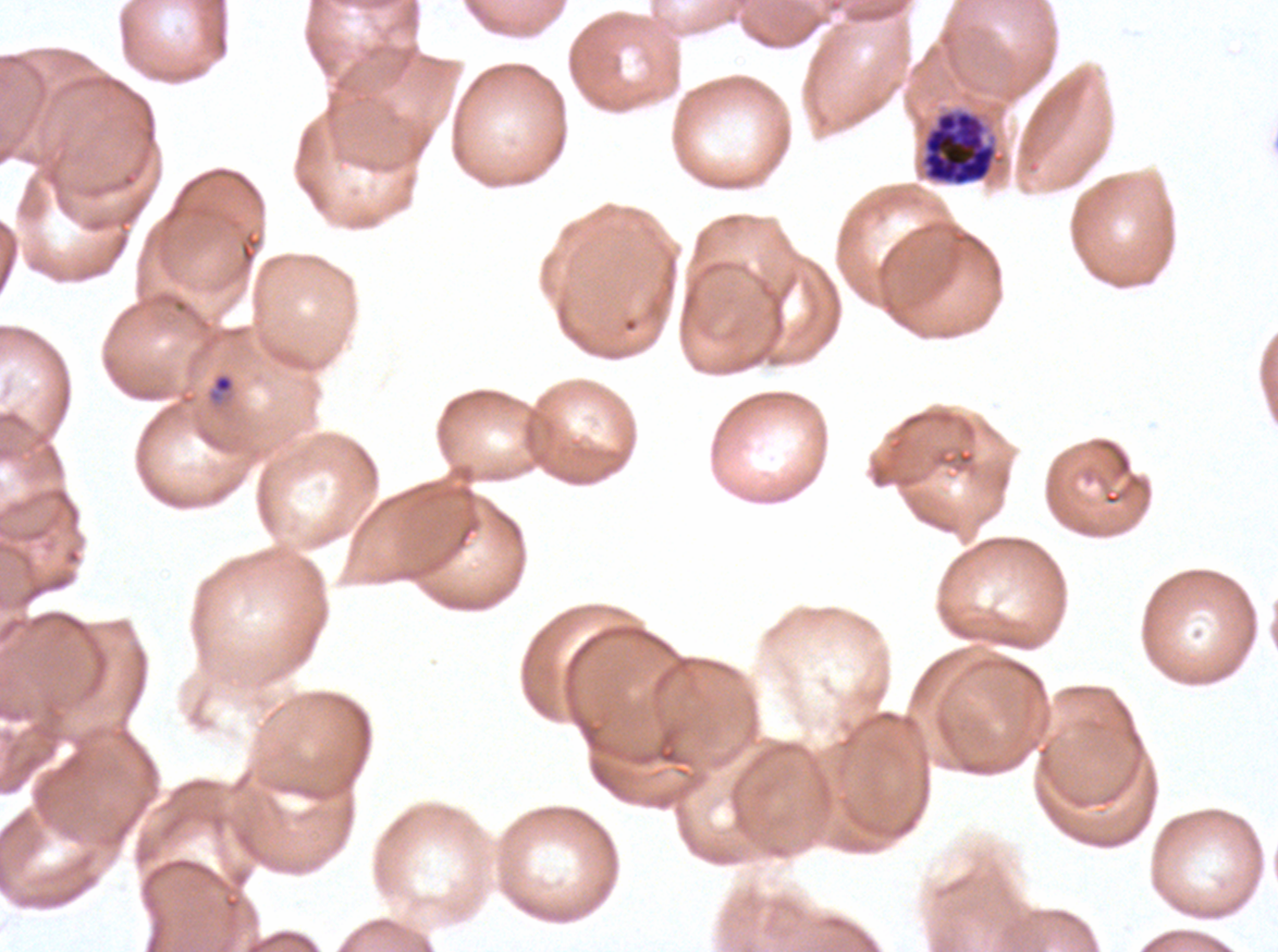
ring_locations: 'approximate bounding boxes as (x1, y1, x2, y2) in pixels: (208, 372, 235, 403)'
stain: Giemsa
preparation: thin blood film
field_of_view: sub-image separated from a larger composite
image_size: 1278×952 pixels
life_cycle_stages_observed: ring, late schizont
specimen: ex-vivo Plasmodium falciparum culture from a patient in The Gambia, grown for 24 to 48 hours
late_schizont_locations: 'approximate bounding boxes as (x1, y1, x2, y2) in pixels: (922, 110, 996, 186)'